Describe the morphology of the erythrocytes.
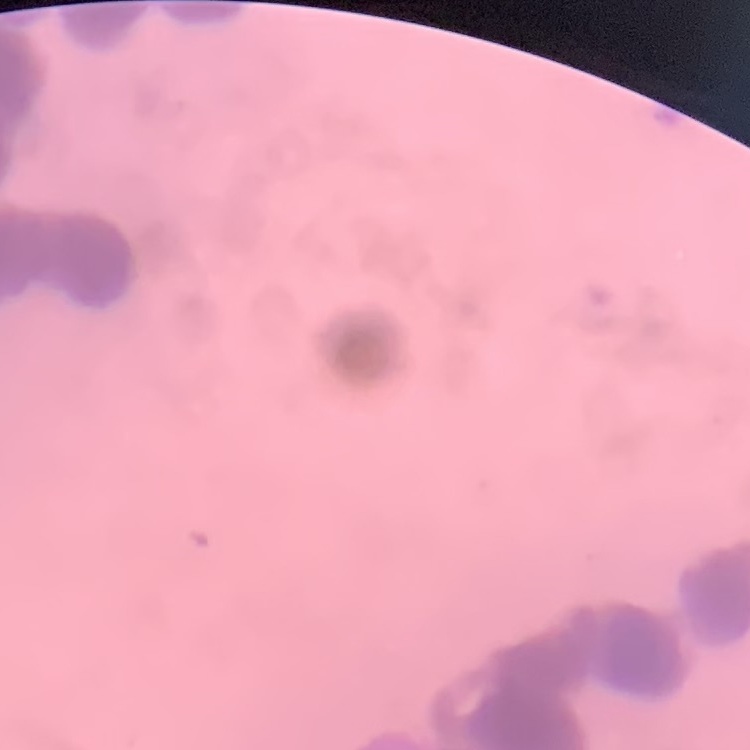
They show rouleaux formation.

Summary:
  - Image type: one tile cut from a larger photomicrograph
  - Preparation: thin blood film
  - Stain: Field's or Giemsa